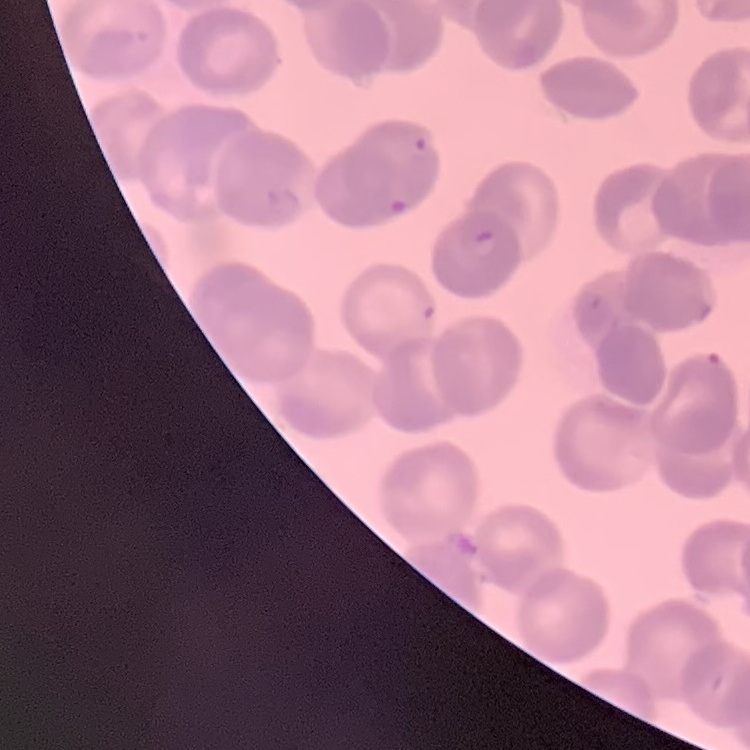

The erythrocytes exhibit rouleaux formation. Square crop of a larger photomicrograph. Thin blood film. Field's or Giemsa stain.